Comment on the morphology of the erythrocytes.
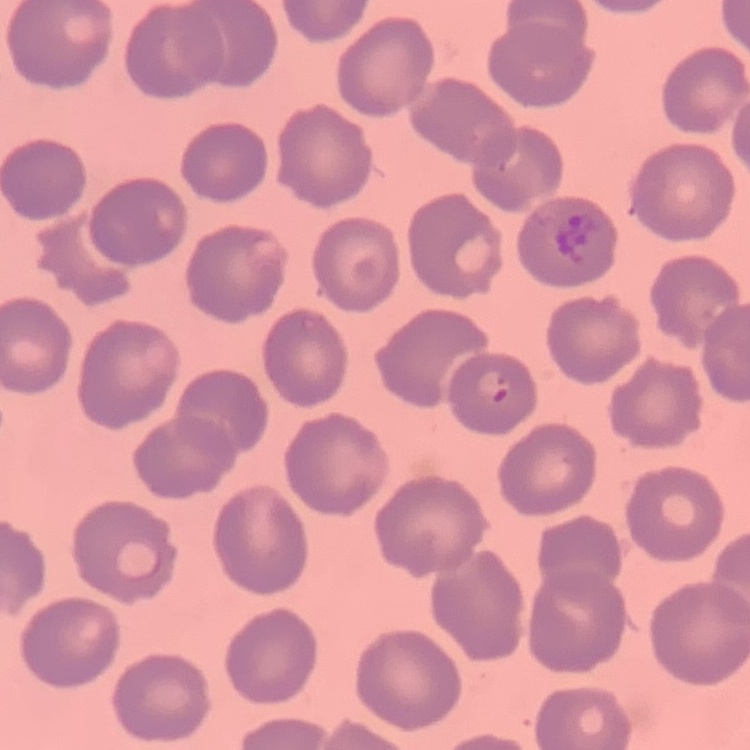
They show no rouleaux formation.

preparation: thin peripheral smear
stain: Field's or Giemsa
image_type: square crop of a larger photomicrograph